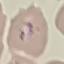

result: malaria parasites detected
preparation: thin blood film
capture: smartphone through the microscope eyepiece
image_type: cell patch, automatically extracted from a larger field of view and resized to 64 × 64 pixels
stain: Giemsa